Assess this cell for malaria.
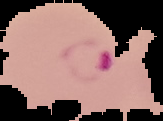
It is parasitized.

Image is 163×121 pixels. From a thin blood smear. Segmented cell region on a black background.